State the blood parasite species.
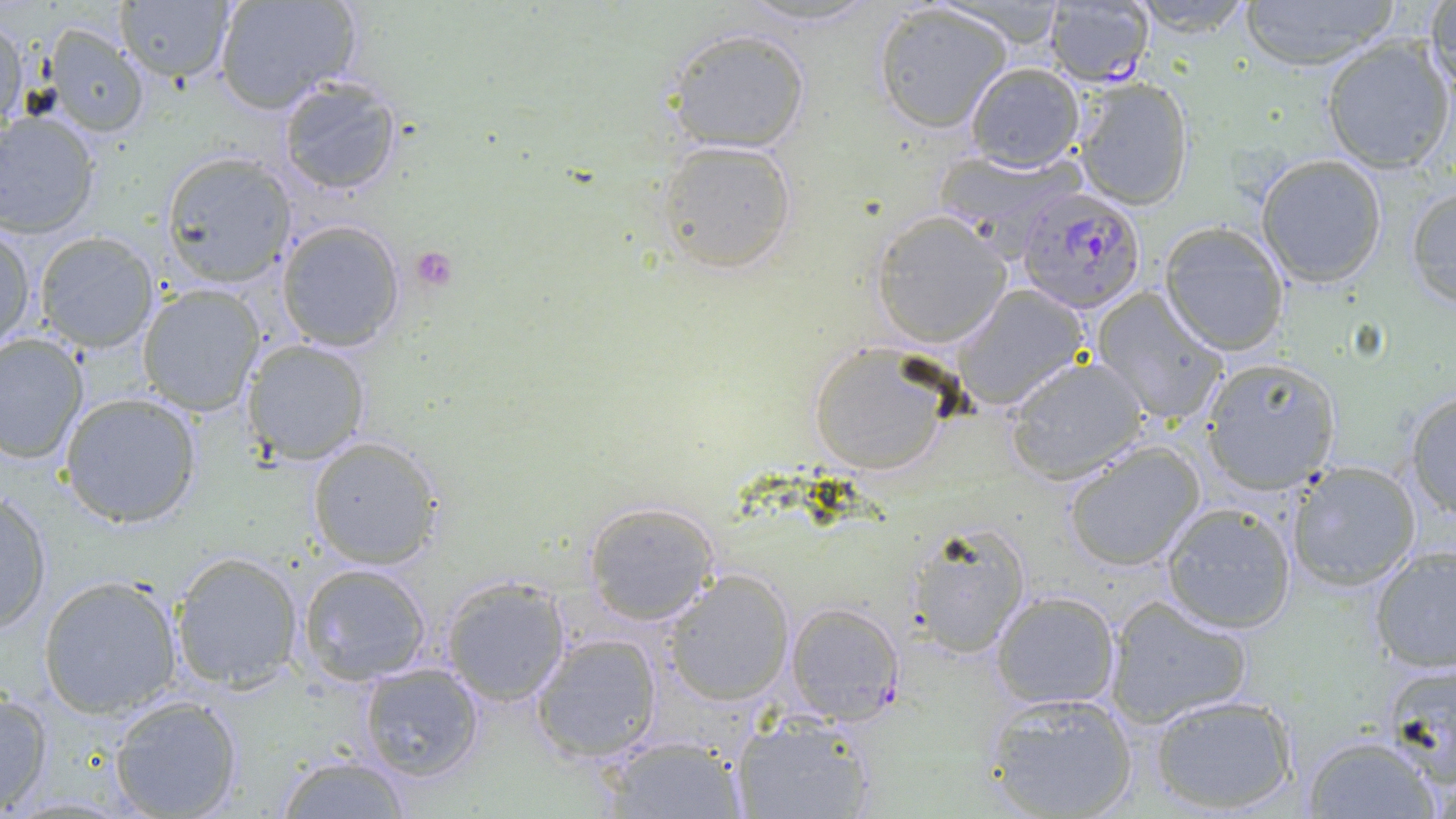

Plasmodium falciparum.

{
  "image_size": "1456×819 pixels",
  "modality": "optical microscopy",
  "platelet_locations": "approximate bounding boxes as [x1, y1, x2, y2] in pixels: [407, 246, 459, 292]",
  "magnification": "1000x",
  "preparation": "thin blood smear",
  "plasmodium_falciparum_infected_red_blood_cell_locations": "approximate bounding boxes as [x1, y1, x2, y2] in pixels: [1041, 1, 1156, 88], [1016, 191, 1148, 313], [784, 598, 906, 725]",
  "field_of_view": "one of a larger specimen",
  "uninfected_red_blood_cell_locations": "approximate bounding boxes as [x1, y1, x2, y2] in pixels: [213, 0, 364, 114], [732, 0, 885, 30], [1128, 0, 1259, 38], [1239, 0, 1397, 70], [1426, 0, 1456, 100], [116, 1, 237, 86], [873, 4, 1012, 132], [0, 14, 29, 135], [38, 24, 152, 138], [665, 28, 809, 154], [1319, 36, 1454, 173], [965, 62, 1085, 171], [1074, 77, 1194, 209], [276, 78, 405, 197], [0, 111, 101, 238], [655, 141, 797, 275], [932, 150, 1088, 260], [159, 152, 298, 288], [1254, 152, 1387, 288], [1405, 185, 1456, 309], [870, 212, 1011, 348], [275, 219, 407, 352], [1159, 222, 1290, 356], [1, 224, 37, 354], [33, 231, 160, 353], [137, 283, 267, 415], [954, 286, 1092, 411], [1090, 288, 1229, 427], [0, 332, 89, 466], [241, 339, 372, 466], [807, 344, 952, 479], [1004, 355, 1151, 482], [1199, 356, 1343, 496], [1404, 390, 1456, 519], [59, 392, 203, 529], [306, 436, 445, 571], [1065, 441, 1206, 571], [1282, 459, 1426, 592], [1, 491, 53, 634], [582, 498, 722, 625], [1158, 500, 1298, 634], [906, 521, 1032, 659], [1369, 545, 1456, 673], [169, 551, 304, 694], [296, 561, 433, 686], [662, 569, 796, 705], [38, 573, 185, 720], [439, 574, 571, 706], [990, 590, 1120, 709], [1105, 596, 1253, 728], [531, 635, 663, 762], [1383, 660, 1455, 795], [356, 663, 486, 784], [0, 688, 54, 813], [982, 690, 1138, 819], [1148, 693, 1297, 815], [108, 696, 243, 819], [729, 714, 877, 819], [600, 732, 746, 817], [1300, 734, 1441, 819], [276, 754, 412, 818]",
  "stain": "May-Grünwald-Giemsa"
}